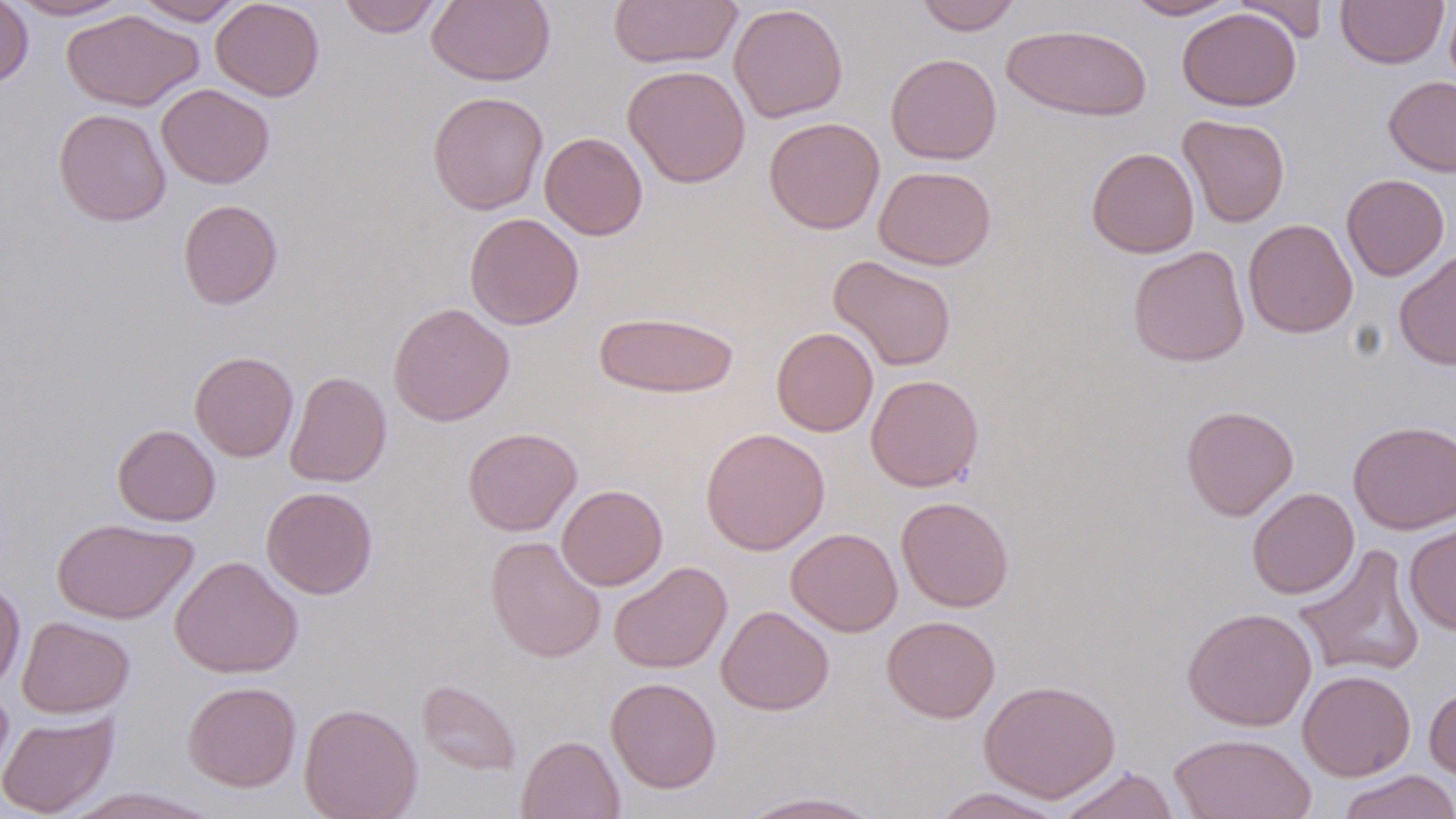
slide-level diagnosis = negative for blood parasites
modality = optical microscopy
uninfected red blood cell locations = approximate bounding boxes as [x1, y1, x2, y2] in pixels: [0, 0, 34, 88], [5, 0, 133, 21], [132, 0, 246, 24], [210, 0, 325, 101], [337, 0, 446, 38], [427, 0, 555, 86], [608, 0, 741, 69], [915, 0, 1022, 34], [1124, 0, 1241, 20], [1234, 0, 1329, 44], [1336, 0, 1449, 68], [729, 3, 849, 123], [1177, 7, 1301, 111], [62, 10, 204, 111], [1001, 24, 1152, 121], [886, 52, 1002, 165], [623, 65, 751, 188], [1383, 76, 1456, 176], [156, 84, 274, 189], [427, 91, 549, 215], [54, 108, 171, 226], [1178, 115, 1290, 227], [763, 117, 885, 234], [539, 131, 648, 240], [1086, 147, 1199, 258], [874, 165, 997, 270], [1341, 174, 1450, 281], [178, 199, 283, 309], [464, 213, 584, 331], [1243, 218, 1358, 338], [1128, 245, 1250, 367], [1395, 249, 1456, 371], [828, 255, 957, 372], [388, 302, 515, 426], [594, 310, 739, 398], [771, 326, 878, 437], [190, 351, 298, 461], [284, 370, 391, 488], [865, 374, 983, 492], [1181, 405, 1299, 521], [1348, 420, 1456, 534], [112, 424, 221, 526], [463, 427, 582, 536], [700, 428, 830, 555], [556, 484, 667, 590], [261, 486, 378, 600], [1247, 487, 1359, 599], [896, 496, 1014, 612], [52, 517, 197, 624], [1404, 521, 1456, 635], [786, 528, 903, 636], [485, 536, 606, 663], [1293, 543, 1427, 679], [169, 556, 303, 678], [609, 561, 732, 674], [0, 579, 25, 692], [716, 605, 834, 715], [1182, 607, 1317, 731], [882, 615, 1000, 723], [16, 616, 135, 718], [1297, 670, 1416, 781], [605, 676, 721, 794], [417, 679, 522, 776], [979, 679, 1120, 802], [182, 680, 301, 792], [1424, 683, 1456, 782], [0, 687, 15, 792], [299, 703, 422, 819], [0, 711, 119, 818], [1168, 732, 1317, 819], [516, 735, 625, 819], [1055, 766, 1180, 819], [1337, 770, 1456, 819], [62, 787, 220, 818], [929, 787, 1068, 818], [736, 791, 885, 818]
field of view = single
image size = 1456×819 pixels
magnification = 1000x
preparation = thin blood smear
stain = May-Grünwald-Giemsa